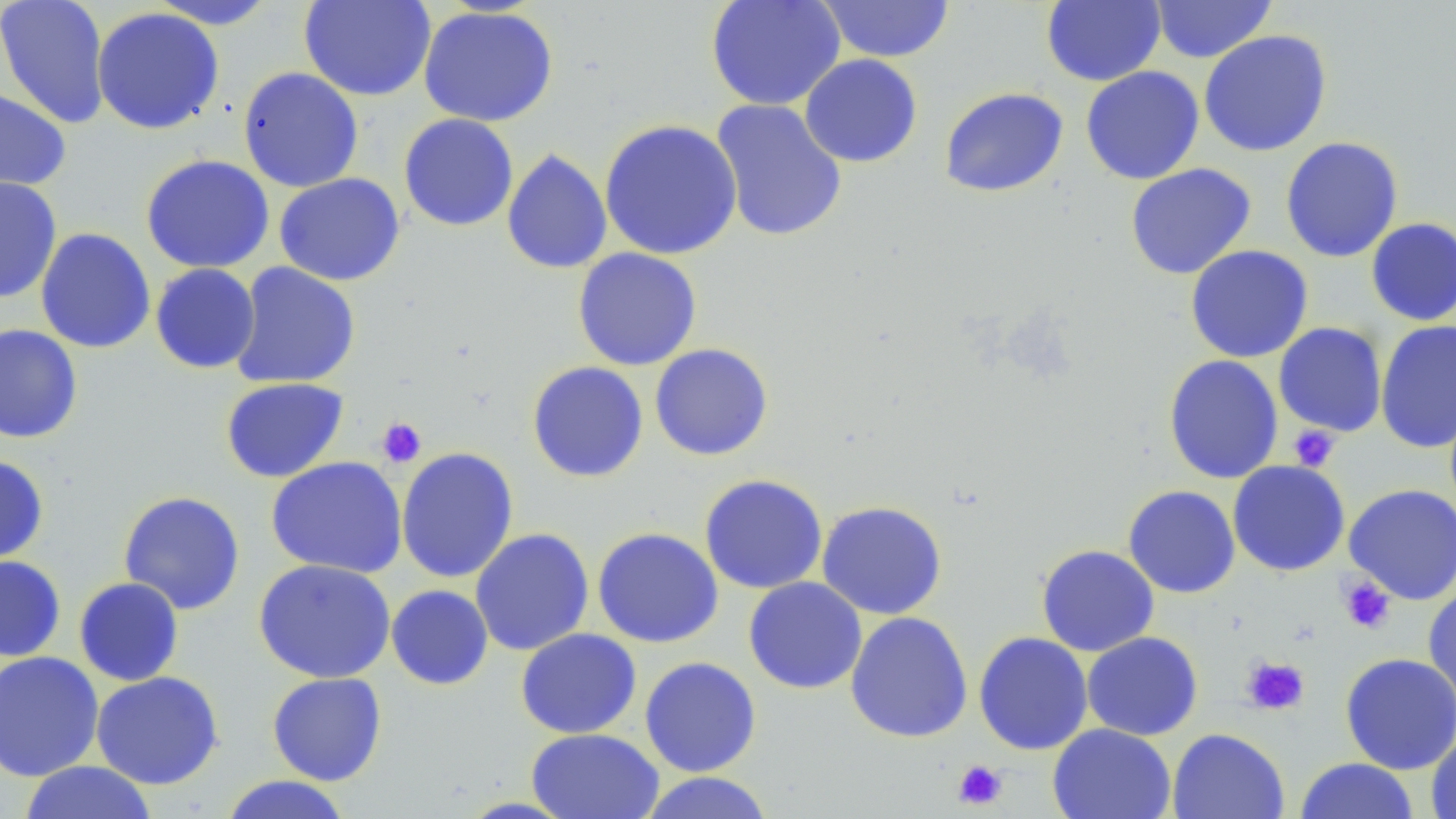
slide-level diagnosis = negative for blood parasites
stain = May-Grünwald-Giemsa
magnification = 1000x
uninfected red blood cell locations = approximate bounding boxes as named x1/y1/x2/y2 corners in pixels: (x1=0, y1=0, x2=111, y2=131), (x1=146, y1=0, x2=281, y2=29), (x1=299, y1=0, x2=437, y2=102), (x1=705, y1=0, x2=846, y2=111), (x1=817, y1=0, x2=956, y2=63), (x1=1041, y1=0, x2=1166, y2=87), (x1=1150, y1=0, x2=1277, y2=63), (x1=418, y1=5, x2=559, y2=127), (x1=92, y1=7, x2=224, y2=135), (x1=1198, y1=29, x2=1332, y2=157), (x1=799, y1=54, x2=923, y2=168), (x1=1080, y1=66, x2=1204, y2=185), (x1=237, y1=67, x2=364, y2=193), (x1=0, y1=87, x2=71, y2=192), (x1=939, y1=87, x2=1069, y2=198), (x1=710, y1=99, x2=848, y2=243), (x1=398, y1=113, x2=519, y2=232), (x1=599, y1=119, x2=743, y2=261), (x1=1280, y1=136, x2=1403, y2=263), (x1=501, y1=148, x2=612, y2=275), (x1=140, y1=154, x2=275, y2=273), (x1=1125, y1=163, x2=1256, y2=280), (x1=273, y1=173, x2=406, y2=286), (x1=0, y1=177, x2=62, y2=303), (x1=1365, y1=218, x2=1456, y2=326), (x1=35, y1=227, x2=156, y2=354), (x1=1185, y1=244, x2=1314, y2=363), (x1=572, y1=247, x2=702, y2=371), (x1=229, y1=262, x2=361, y2=389), (x1=150, y1=263, x2=261, y2=374), (x1=1375, y1=320, x2=1456, y2=454), (x1=1273, y1=322, x2=1388, y2=437), (x1=0, y1=323, x2=84, y2=444), (x1=649, y1=343, x2=774, y2=461), (x1=1163, y1=354, x2=1284, y2=484), (x1=526, y1=361, x2=649, y2=482), (x1=219, y1=377, x2=349, y2=483), (x1=395, y1=447, x2=519, y2=583), (x1=0, y1=454, x2=49, y2=564), (x1=265, y1=456, x2=408, y2=578), (x1=1227, y1=460, x2=1350, y2=576), (x1=698, y1=473, x2=828, y2=594), (x1=1343, y1=483, x2=1456, y2=605), (x1=1123, y1=485, x2=1240, y2=599), (x1=118, y1=490, x2=245, y2=615), (x1=816, y1=500, x2=948, y2=619), (x1=592, y1=527, x2=724, y2=649), (x1=470, y1=528, x2=595, y2=656), (x1=1036, y1=544, x2=1159, y2=656), (x1=0, y1=554, x2=66, y2=661), (x1=253, y1=558, x2=396, y2=683), (x1=743, y1=576, x2=867, y2=695), (x1=73, y1=577, x2=185, y2=687), (x1=1423, y1=582, x2=1456, y2=708), (x1=386, y1=584, x2=494, y2=690), (x1=845, y1=611, x2=973, y2=744), (x1=515, y1=628, x2=642, y2=739), (x1=1081, y1=631, x2=1203, y2=741), (x1=973, y1=632, x2=1093, y2=755), (x1=0, y1=651, x2=104, y2=782), (x1=1340, y1=652, x2=1456, y2=774), (x1=639, y1=656, x2=762, y2=777), (x1=90, y1=671, x2=224, y2=790), (x1=266, y1=672, x2=387, y2=786), (x1=1048, y1=723, x2=1176, y2=819), (x1=526, y1=728, x2=664, y2=819), (x1=1167, y1=728, x2=1290, y2=819), (x1=1426, y1=732, x2=1456, y2=819), (x1=1294, y1=757, x2=1420, y2=818), (x1=18, y1=761, x2=159, y2=819), (x1=638, y1=771, x2=776, y2=819), (x1=218, y1=775, x2=355, y2=819)
preparation = thin blood film
image size = 1456×819 pixels
modality = optical microscopy
platelet locations = approximate bounding boxes as named x1/y1/x2/y2 corners in pixels: (x1=376, y1=417, x2=427, y2=468), (x1=1288, y1=425, x2=1340, y2=471), (x1=1337, y1=575, x2=1396, y2=634), (x1=1241, y1=656, x2=1310, y2=715), (x1=953, y1=759, x2=1007, y2=810)
field of view = single